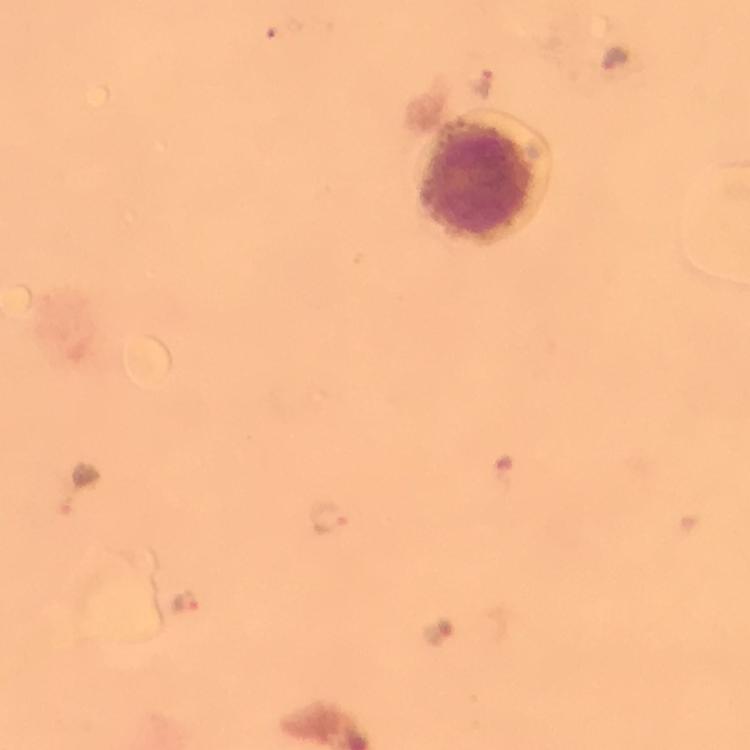

Approximate centers as {x, y} in pixels. Plasmodium parasite locations: {483, 82}, {80, 487}, {329, 518}, {186, 599}. Photographed through the microscope with a smartphone camera. Giemsa stain. From a malaria diagnostic workup. Thick smear. Image is 750×750 pixels. Immersion oil applied. At 100x magnification. A crop from one field of view.